Comment on the morphology of the erythrocytes.
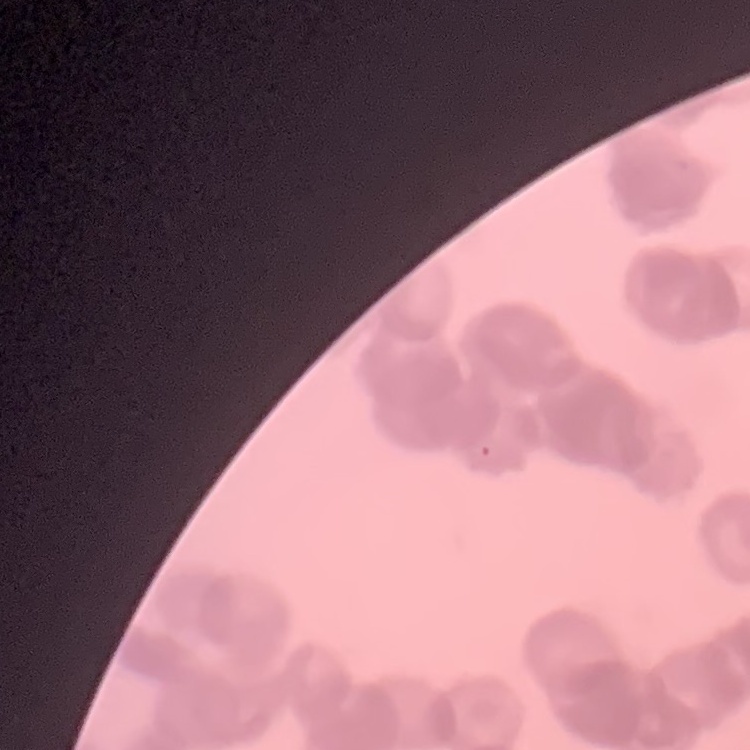

Rouleaux formation.

stain = Field's or Giemsa
preparation = thin peripheral smear
image type = one tile cut from a larger photomicrograph